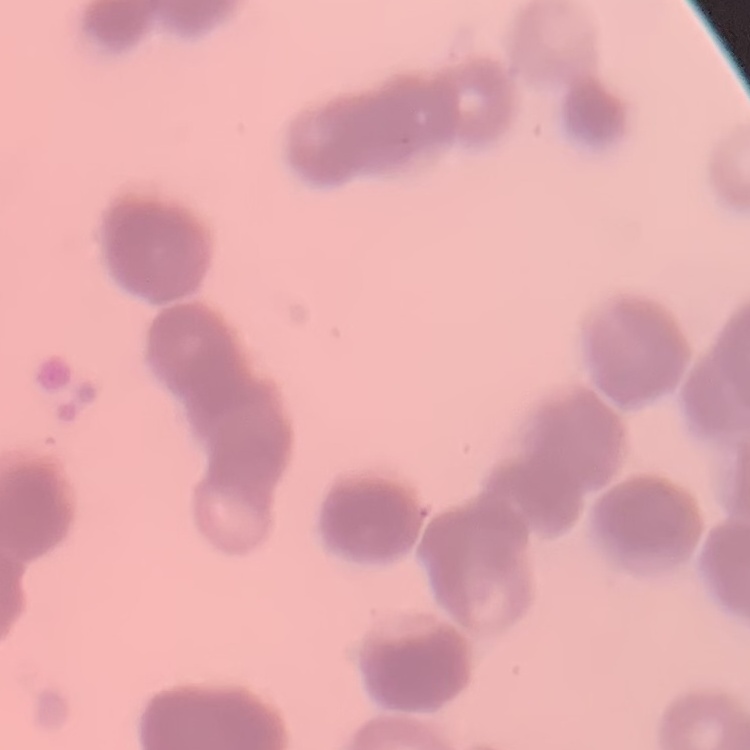

{
  "erythrocyte_morphology": "rouleaux formation",
  "image_type": "one tile cut from a larger photomicrograph",
  "stain": "Field's or Giemsa",
  "preparation": "thin blood smear"
}